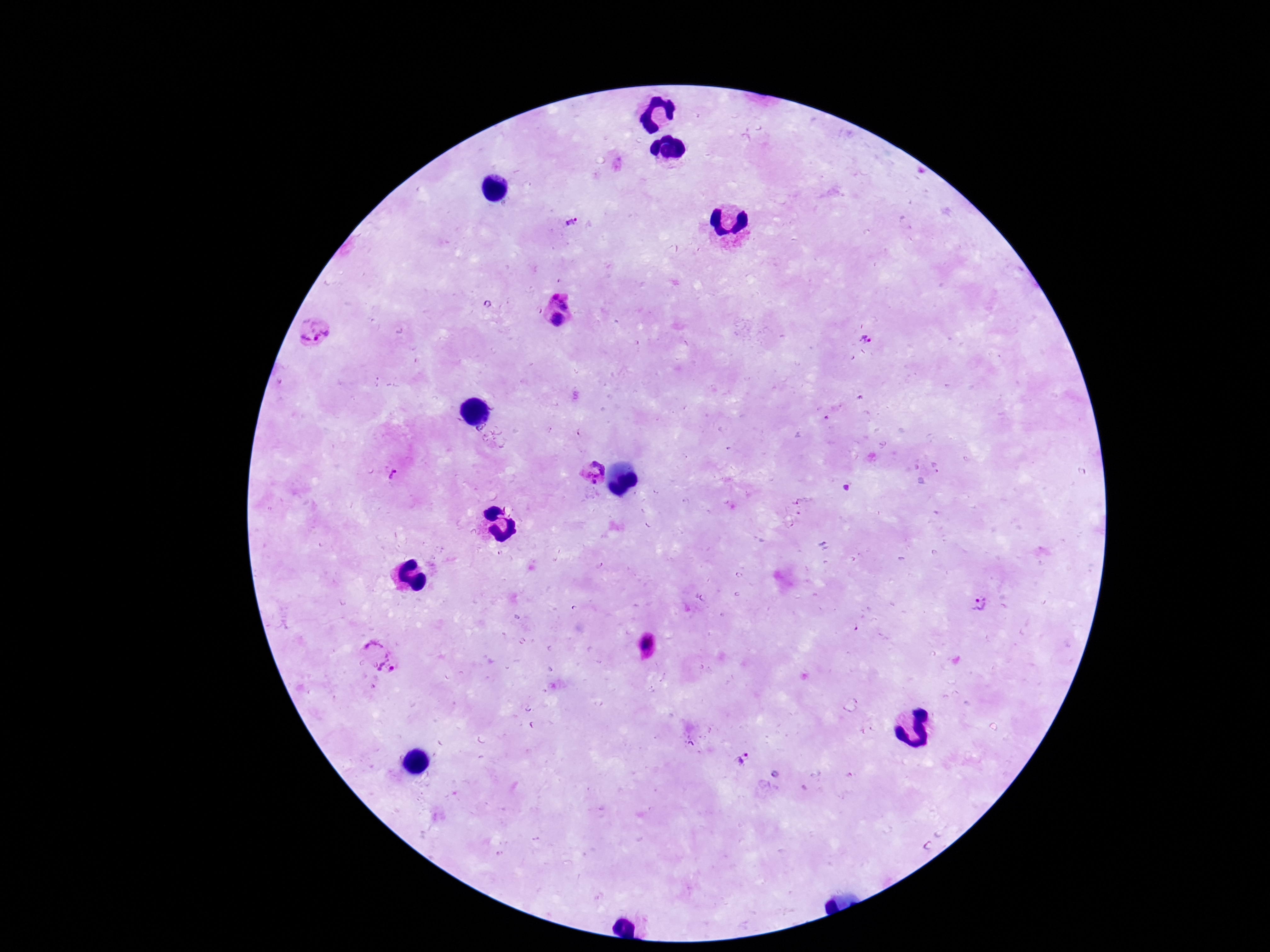
Approximate centers as (x, y) in pixels. Plasmodium parasite locations: (572, 223), (558, 309), (316, 333), (866, 340), (590, 471), (389, 478), (977, 604), (646, 647), (381, 655), (743, 756). Image is 1270×952 pixels. Patient malaria status: positive. Giemsa stain. 100x magnification. Single field of view. Thick blood smear. Smartphone photograph taken through the microscope eyepiece.